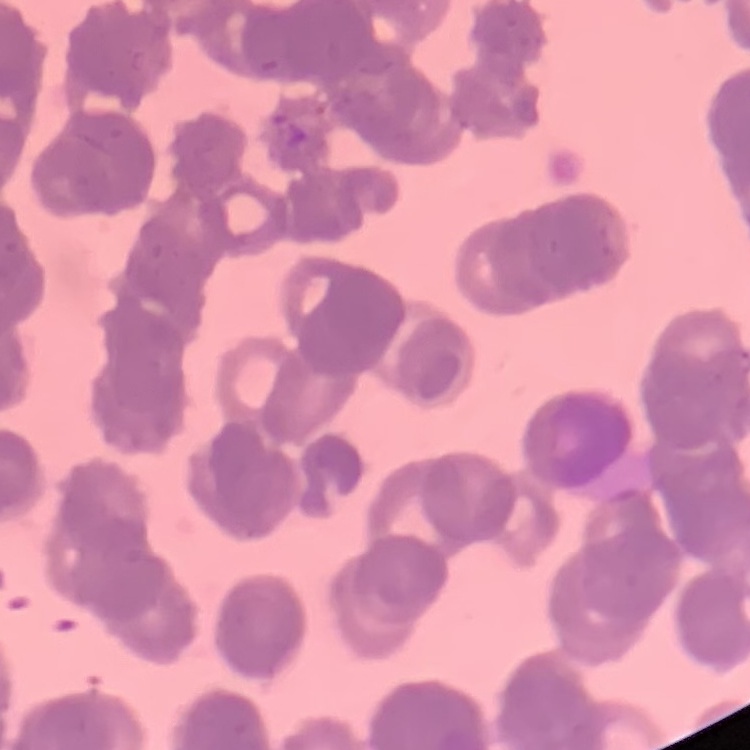
{
  "erythrocyte_morphology": "rouleaux formation",
  "preparation": "thin peripheral smear",
  "stain": "Field's or Giemsa",
  "image_type": "one tile cut from a larger photomicrograph"
}